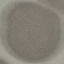
result = no malaria parasites detected
preparation = thin blood smear
capture = smartphone camera at the microscope eyepiece
stain = Giemsa
image type = automatically extracted cell patch, resized to 64 × 64 pixels